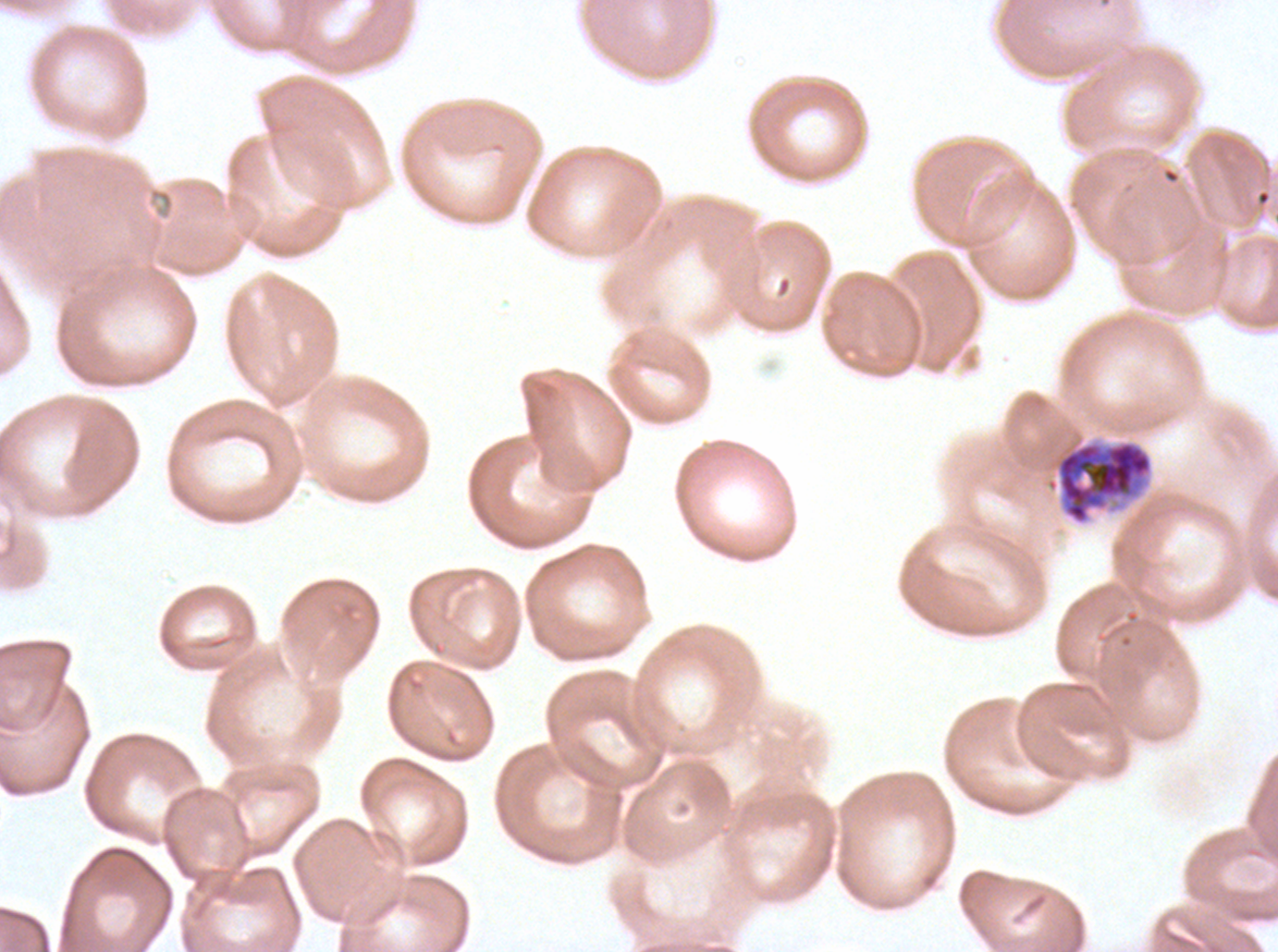
Approximate bounding rectangles given as corner coordinates in pixels from the top-left.
Summary:
  - Early schizont locations: (x1=1046, y1=439, x2=1153, y2=526)
  - Stain: Giemsa
  - Image size: 1278×952 pixels
  - Field of view: one sub-image of a larger composite
  - Specimen: Plasmodium falciparum from a patient in The Gambia, cultured ex vivo for 24 to 48 hours
  - Preparation: thin blood film